Locate every Plasmodium ovale-infected red blood cell.
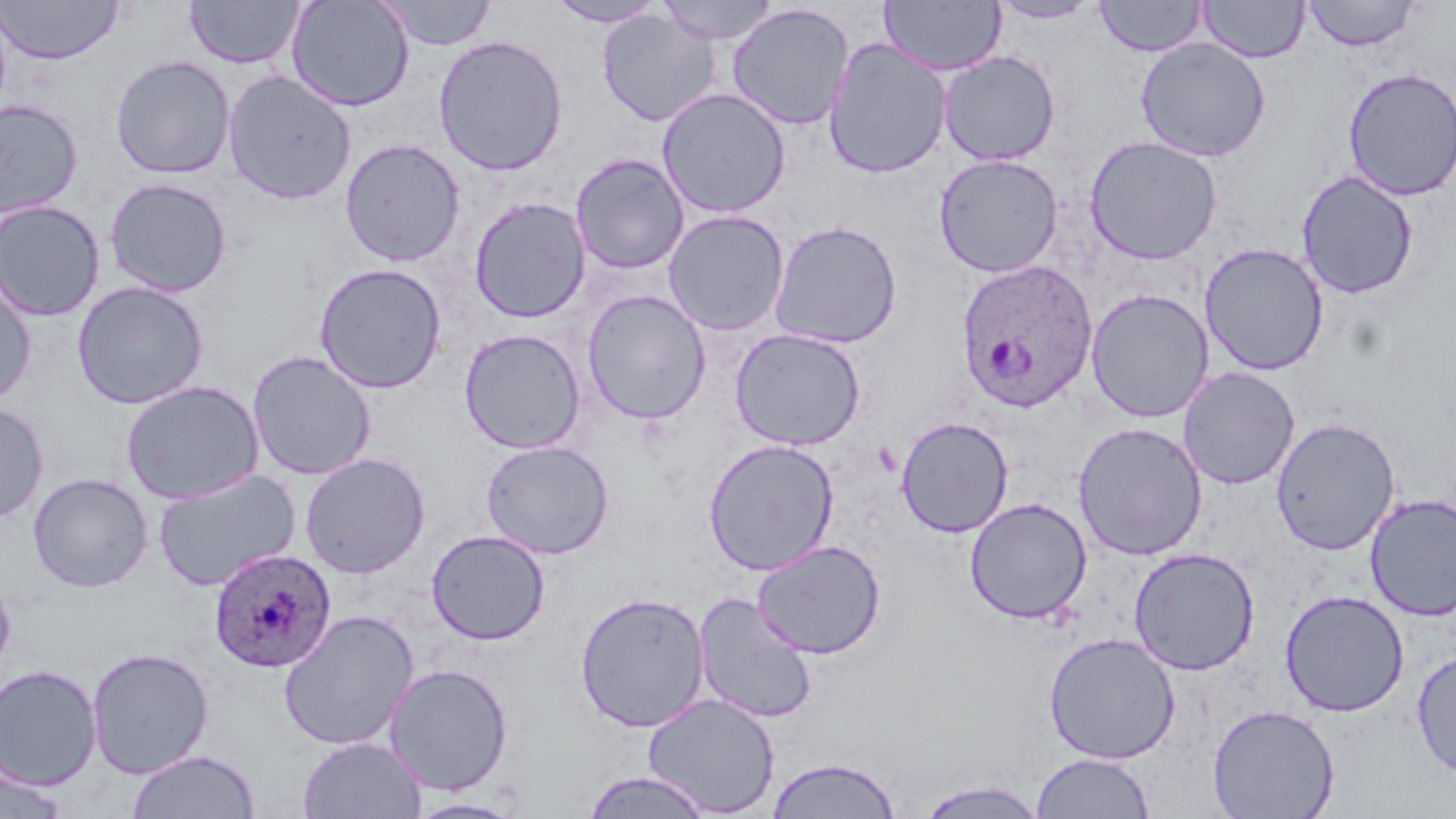
Approximate bounding boxes as named x1/y1/x2/y2 corners in pixels.
Plasmodium ovale-infected red blood cells: (x1=956, y1=260, x2=1099, y2=414), (x1=208, y1=546, x2=337, y2=672).

slide-level diagnosis = Plasmodium ovale
preparation = thin blood smear
stain = May-Grünwald-Giemsa
modality = optical microscopy
uninfected red blood cell locations = approximate bounding boxes as named x1/y1/x2/y2 corners in pixels: (x1=0, y1=0, x2=125, y2=64), (x1=286, y1=0, x2=415, y2=112), (x1=378, y1=0, x2=497, y2=50), (x1=546, y1=0, x2=667, y2=27), (x1=657, y1=0, x2=779, y2=45), (x1=1094, y1=0, x2=1208, y2=57), (x1=1199, y1=0, x2=1310, y2=63), (x1=185, y1=1, x2=304, y2=69), (x1=879, y1=1, x2=1006, y2=76), (x1=988, y1=1, x2=1102, y2=24), (x1=1301, y1=1, x2=1421, y2=51), (x1=726, y1=3, x2=854, y2=131), (x1=597, y1=10, x2=721, y2=127), (x1=433, y1=34, x2=568, y2=176), (x1=822, y1=37, x2=951, y2=179), (x1=1135, y1=38, x2=1271, y2=162), (x1=938, y1=50, x2=1061, y2=165), (x1=111, y1=55, x2=235, y2=179), (x1=1342, y1=67, x2=1456, y2=201), (x1=222, y1=70, x2=356, y2=205), (x1=657, y1=87, x2=791, y2=218), (x1=0, y1=99, x2=84, y2=219), (x1=1084, y1=135, x2=1222, y2=265), (x1=339, y1=138, x2=465, y2=267), (x1=570, y1=153, x2=689, y2=274), (x1=933, y1=154, x2=1063, y2=277), (x1=1296, y1=170, x2=1419, y2=300), (x1=105, y1=177, x2=232, y2=298), (x1=0, y1=196, x2=232, y2=312), (x1=468, y1=197, x2=592, y2=324), (x1=0, y1=200, x2=104, y2=322), (x1=663, y1=210, x2=790, y2=336), (x1=769, y1=220, x2=903, y2=348), (x1=1199, y1=243, x2=1328, y2=376), (x1=314, y1=262, x2=448, y2=394), (x1=0, y1=277, x2=36, y2=409), (x1=72, y1=281, x2=208, y2=409), (x1=1085, y1=289, x2=1214, y2=423), (x1=582, y1=290, x2=711, y2=425), (x1=729, y1=328, x2=866, y2=450), (x1=459, y1=329, x2=586, y2=454), (x1=247, y1=350, x2=376, y2=481), (x1=1178, y1=367, x2=1300, y2=490), (x1=121, y1=380, x2=264, y2=504), (x1=0, y1=402, x2=49, y2=523), (x1=895, y1=416, x2=1014, y2=538), (x1=1269, y1=417, x2=1401, y2=556), (x1=1073, y1=421, x2=1208, y2=561), (x1=703, y1=438, x2=840, y2=575), (x1=480, y1=440, x2=615, y2=559), (x1=299, y1=452, x2=431, y2=578), (x1=152, y1=469, x2=301, y2=592), (x1=28, y1=472, x2=153, y2=593), (x1=1364, y1=493, x2=1456, y2=621), (x1=964, y1=498, x2=1092, y2=624), (x1=426, y1=530, x2=550, y2=645), (x1=751, y1=539, x2=886, y2=660), (x1=1128, y1=547, x2=1260, y2=676), (x1=0, y1=571, x2=15, y2=676), (x1=1279, y1=589, x2=1410, y2=717), (x1=574, y1=591, x2=710, y2=732), (x1=694, y1=592, x2=818, y2=724), (x1=278, y1=609, x2=419, y2=750), (x1=1043, y1=632, x2=1181, y2=764), (x1=86, y1=646, x2=214, y2=779), (x1=1411, y1=649, x2=1456, y2=780), (x1=0, y1=663, x2=102, y2=791), (x1=384, y1=663, x2=514, y2=796), (x1=642, y1=693, x2=780, y2=817), (x1=1207, y1=704, x2=1340, y2=819), (x1=297, y1=736, x2=426, y2=819), (x1=126, y1=749, x2=261, y2=818), (x1=1031, y1=752, x2=1155, y2=818), (x1=766, y1=755, x2=902, y2=819), (x1=0, y1=762, x2=70, y2=818), (x1=580, y1=770, x2=716, y2=818), (x1=913, y1=779, x2=1049, y2=819), (x1=406, y1=797, x2=527, y2=818)
magnification = 1000x
image size = 1456×819 pixels
field of view = one of a larger specimen